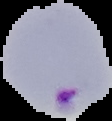 Malaria status: parasitized. From a thin blood smear. Image is 112×121 pixels. Segmented cell region on a black background.